Report the malaria status of this cell.
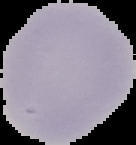
Uninfected.

image type = segmented cell region on a black background
image size = 136×145 pixels
preparation = thin blood smear